Classify this cell by malaria status.
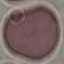

It is uninfected.

Cell patch, automatically extracted from a larger field of view and resized to 64 × 64 pixels. Thin smear of blood. Acquired by smartphone through the microscope eyepiece. Giemsa-stained preparation.